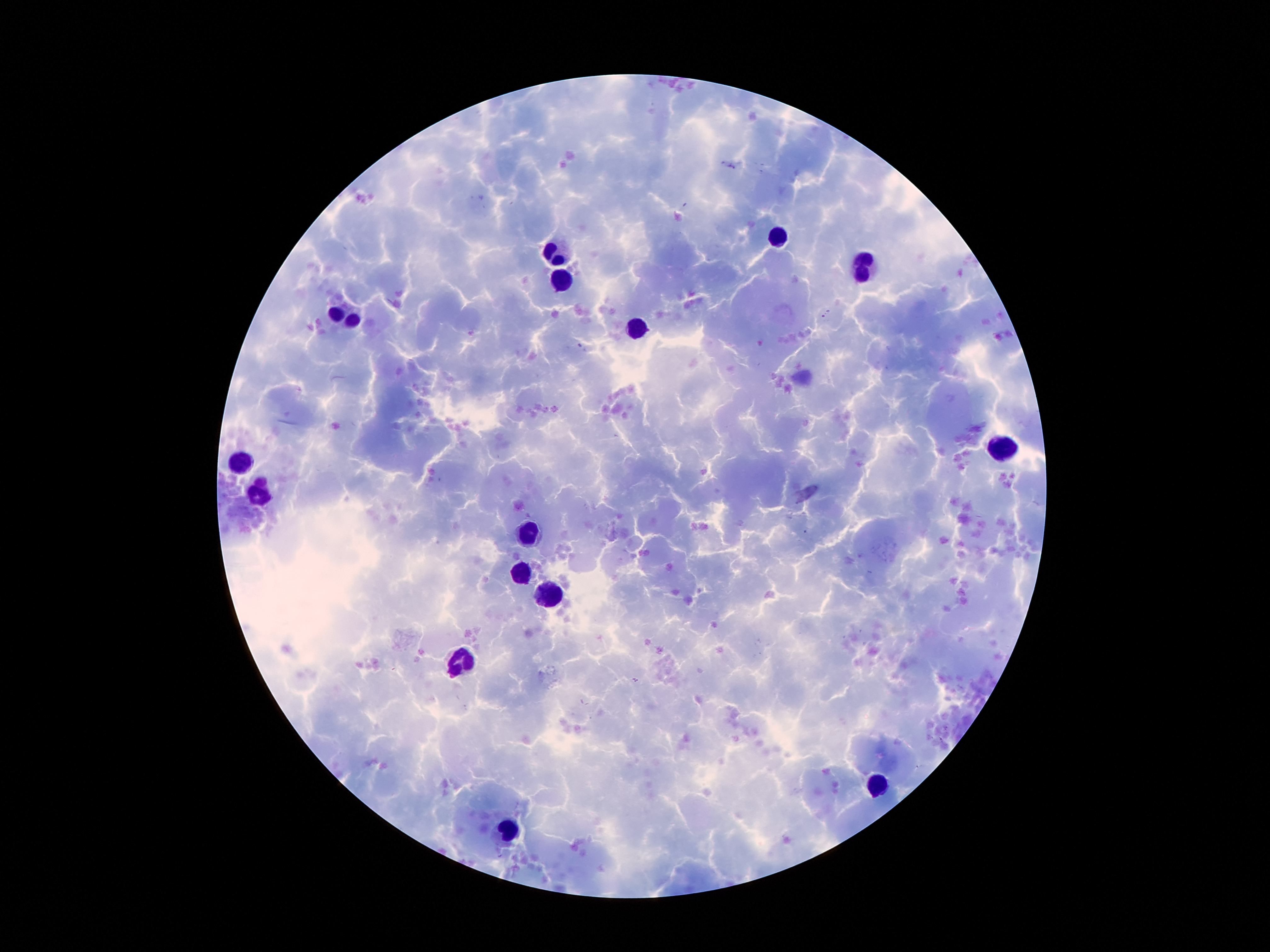

Approximate centers as [x, y] in pixels.
Summary:
  - Leukocyte locations: [779, 234], [553, 256], [866, 266], [562, 282], [349, 315], [639, 326], [1003, 445], [244, 458], [262, 489], [529, 531], [524, 572], [548, 595], [461, 661], [880, 784], [509, 832]
  - Field of view: single
  - Patient malaria status: positive for Plasmodium falciparum
  - Preparation: thick peripheral-blood smear
  - Magnification: 100x
  - Image size: 1270×952 pixels
  - Capture: smartphone through the microscope eyepiece
  - Malaria parasites: not detected
  - Stain: Giemsa